Assess for Plasmodium parasites.
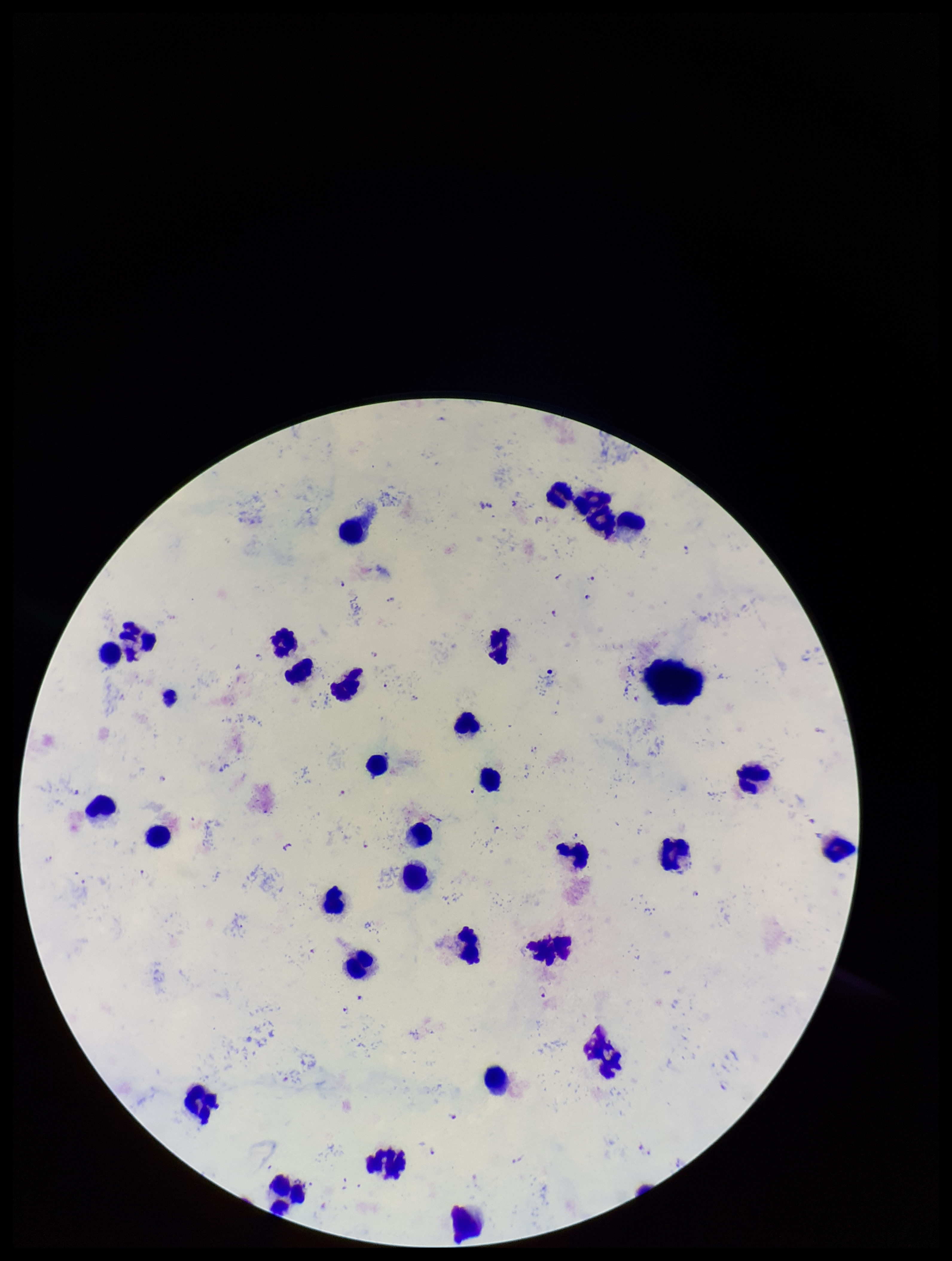
Detected.

Preparation: thick blood smear. Smartphone photograph taken through the eyepiece of a microscope. Patient malaria status: infected. Species reported for this patient: Plasmodium falciparum. Leukocyte count: 33. Parasite count: 16. Image is 952×1261 pixels. One field from this slide. Stained with Giemsa.